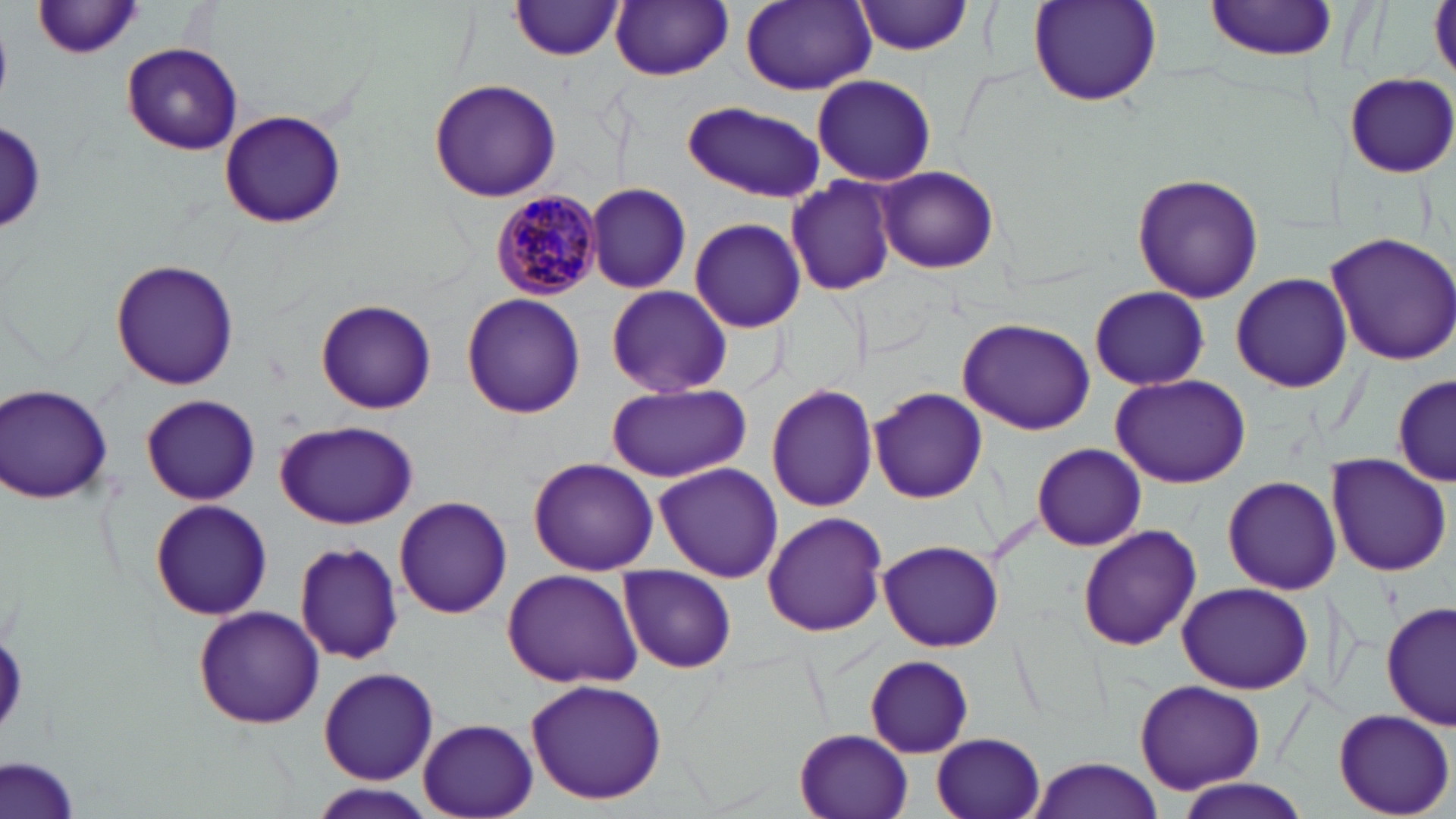

slide_level_diagnosis: Plasmodium malariae
field_of_view: one of a larger specimen
magnification: 1000x
image_size: 1456×819 pixels
plasmodium_malariae_infected_red_blood_cell_locations: 'approximate bounding boxes as named x1/y1/x2/y2 corners in pixels: (x1=493, y1=191, x2=602, y2=298)'
stain: May-Grünwald-Giemsa
modality: light microscopy
uninfected_red_blood_cell_locations: 'approximate bounding boxes as named x1/y1/x2/y2 corners in pixels: (x1=1028, y1=0, x2=1164, y2=109), (x1=1204, y1=0, x2=1340, y2=61), (x1=512, y1=1, x2=622, y2=59), (x1=612, y1=1, x2=733, y2=80), (x1=740, y1=1, x2=875, y2=94), (x1=856, y1=1, x2=977, y2=55), (x1=1428, y1=1, x2=1456, y2=81), (x1=34, y1=3, x2=149, y2=60), (x1=122, y1=42, x2=243, y2=156), (x1=1346, y1=72, x2=1455, y2=177), (x1=811, y1=74, x2=937, y2=186), (x1=428, y1=78, x2=562, y2=203), (x1=681, y1=102, x2=825, y2=201), (x1=219, y1=110, x2=343, y2=227), (x1=2, y1=121, x2=46, y2=232), (x1=875, y1=165, x2=996, y2=275), (x1=1132, y1=173, x2=1263, y2=303), (x1=786, y1=176, x2=897, y2=294), (x1=586, y1=182, x2=693, y2=294), (x1=688, y1=216, x2=808, y2=333), (x1=1325, y1=231, x2=1456, y2=365), (x1=1233, y1=258, x2=1454, y2=379), (x1=111, y1=259, x2=239, y2=390), (x1=1230, y1=272, x2=1352, y2=393), (x1=605, y1=285, x2=733, y2=398), (x1=1089, y1=287, x2=1209, y2=389), (x1=460, y1=293, x2=586, y2=419), (x1=315, y1=298, x2=437, y2=413), (x1=958, y1=318, x2=1096, y2=434), (x1=1111, y1=373, x2=1249, y2=488), (x1=1394, y1=373, x2=1454, y2=486), (x1=1, y1=384, x2=115, y2=503), (x1=605, y1=384, x2=751, y2=481), (x1=767, y1=385, x2=877, y2=511), (x1=870, y1=388, x2=988, y2=503), (x1=142, y1=395, x2=259, y2=504), (x1=275, y1=421, x2=418, y2=528), (x1=1033, y1=443, x2=1146, y2=551), (x1=1328, y1=455, x2=1453, y2=575), (x1=527, y1=457, x2=659, y2=574), (x1=654, y1=462, x2=783, y2=583), (x1=1223, y1=475, x2=1341, y2=595), (x1=394, y1=496, x2=512, y2=618), (x1=151, y1=499, x2=271, y2=620), (x1=762, y1=511, x2=887, y2=637), (x1=1076, y1=525, x2=1202, y2=651), (x1=875, y1=539, x2=1006, y2=653), (x1=288, y1=540, x2=405, y2=668), (x1=619, y1=564, x2=736, y2=673), (x1=501, y1=568, x2=644, y2=687), (x1=1176, y1=582, x2=1313, y2=695), (x1=1382, y1=601, x2=1456, y2=732), (x1=193, y1=605, x2=325, y2=729), (x1=864, y1=655, x2=975, y2=757), (x1=318, y1=666, x2=439, y2=785), (x1=523, y1=678, x2=668, y2=806), (x1=1133, y1=679, x2=1265, y2=793), (x1=1332, y1=708, x2=1453, y2=817), (x1=416, y1=718, x2=538, y2=818), (x1=795, y1=729, x2=915, y2=818), (x1=931, y1=733, x2=1045, y2=819), (x1=1, y1=756, x2=82, y2=819), (x1=1027, y1=758, x2=1166, y2=819), (x1=1173, y1=780, x2=1313, y2=818), (x1=310, y1=785, x2=438, y2=819)'
preparation: thin blood smear